State which parasite is depicted.
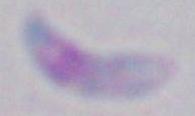

This is Toxoplasma gondii.

magnification: 1000x
modality: micrograph